Locate every Plasmodium falciparum-infected red blood cell.
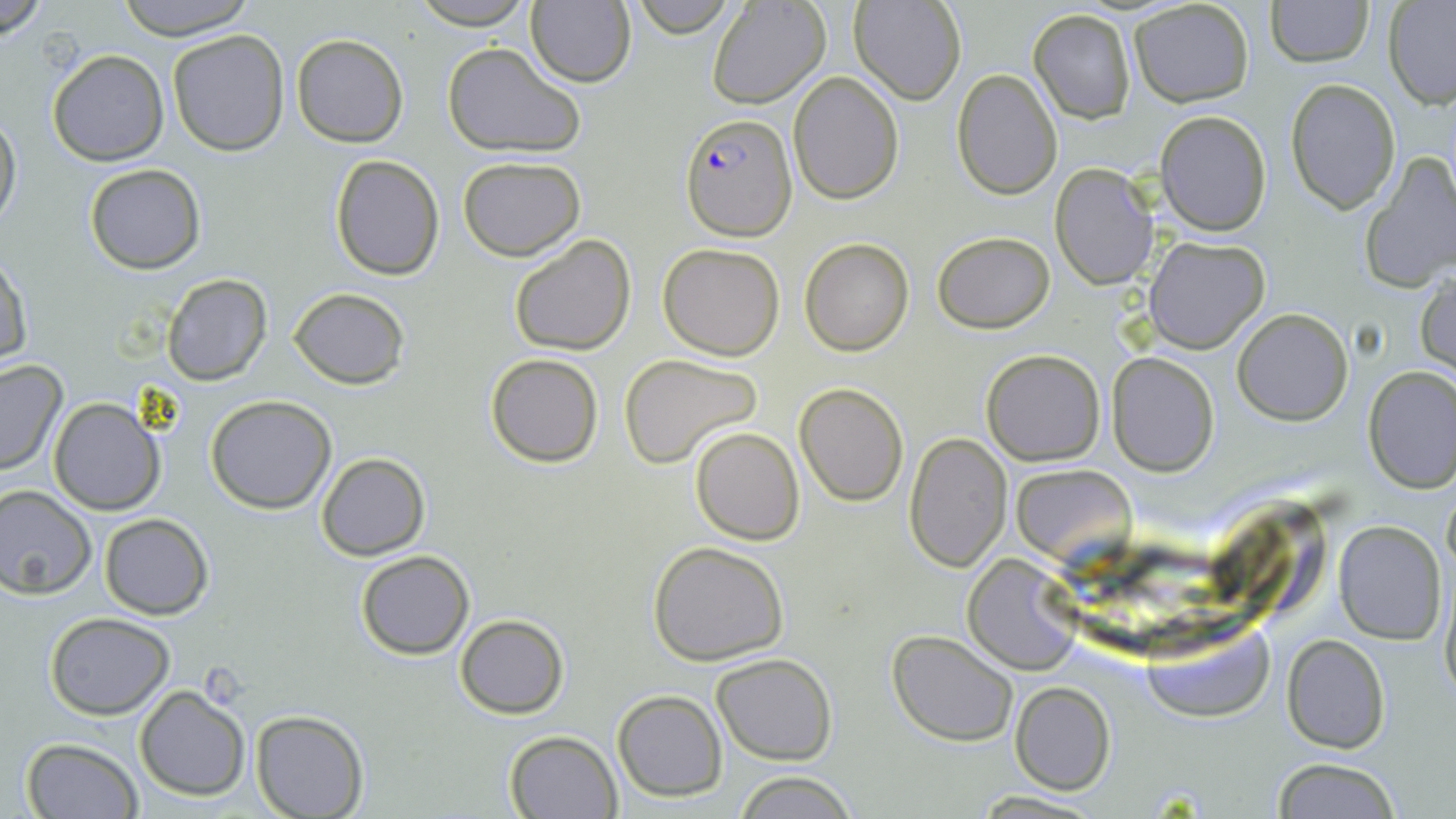

Approximate bounding boxes as [x1, y1, x2, y2] in pixels.
Plasmodium falciparum-infected red blood cells: [679, 111, 797, 242].

Uninfected red blood cell locations: [0, 0, 51, 38], [110, 0, 257, 39], [410, 0, 537, 28], [525, 0, 636, 88], [708, 0, 830, 108], [849, 0, 965, 104], [1263, 0, 1374, 67], [1129, 2, 1255, 109], [1383, 2, 1456, 108], [624, 3, 745, 36], [1028, 9, 1137, 124], [167, 29, 289, 156], [290, 33, 409, 147], [442, 43, 586, 159], [47, 50, 168, 167], [952, 69, 1063, 199], [788, 73, 903, 206], [1285, 78, 1399, 216], [1154, 110, 1271, 235], [0, 112, 21, 232], [1359, 152, 1456, 293], [328, 153, 446, 282], [457, 156, 586, 259], [1051, 164, 1158, 290], [84, 165, 205, 275], [931, 230, 1056, 332], [508, 234, 638, 357], [1144, 236, 1270, 353], [799, 238, 914, 356], [659, 242, 785, 361], [1, 254, 32, 366], [1416, 271, 1456, 374], [162, 274, 272, 386], [287, 287, 410, 388], [1233, 309, 1353, 425], [981, 350, 1106, 465], [1108, 351, 1219, 475], [486, 353, 604, 466], [618, 354, 764, 469], [0, 360, 67, 477], [1363, 366, 1455, 494], [795, 384, 908, 505], [206, 395, 336, 513], [48, 397, 164, 515], [690, 427, 804, 545], [903, 433, 1010, 573], [316, 453, 429, 560], [1010, 464, 1137, 567], [0, 482, 97, 597], [1443, 487, 1456, 577], [1219, 495, 1326, 609], [98, 513, 213, 619], [1334, 520, 1445, 644], [646, 541, 791, 666], [354, 550, 474, 660], [964, 554, 1082, 673], [1439, 574, 1455, 708], [46, 612, 174, 718], [455, 612, 569, 719], [1134, 615, 1274, 723], [888, 629, 1018, 746], [1281, 634, 1390, 754], [712, 654, 837, 766], [1010, 683, 1115, 796], [134, 684, 250, 801], [612, 690, 726, 801], [251, 712, 370, 819], [505, 729, 621, 817], [22, 737, 140, 819], [1271, 758, 1403, 818], [734, 769, 858, 819], [970, 790, 1110, 818]. Slide-level diagnosis: Plasmodium falciparum. Light microscopy. Image is 1456×819 pixels. May-Grünwald-Giemsa stain. Single field of view. 1000x magnification. Thin blood film.